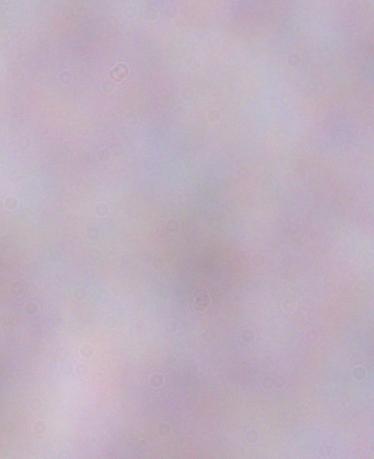 A trypanosome is shown. Micrograph. Captured at 1000x magnification.